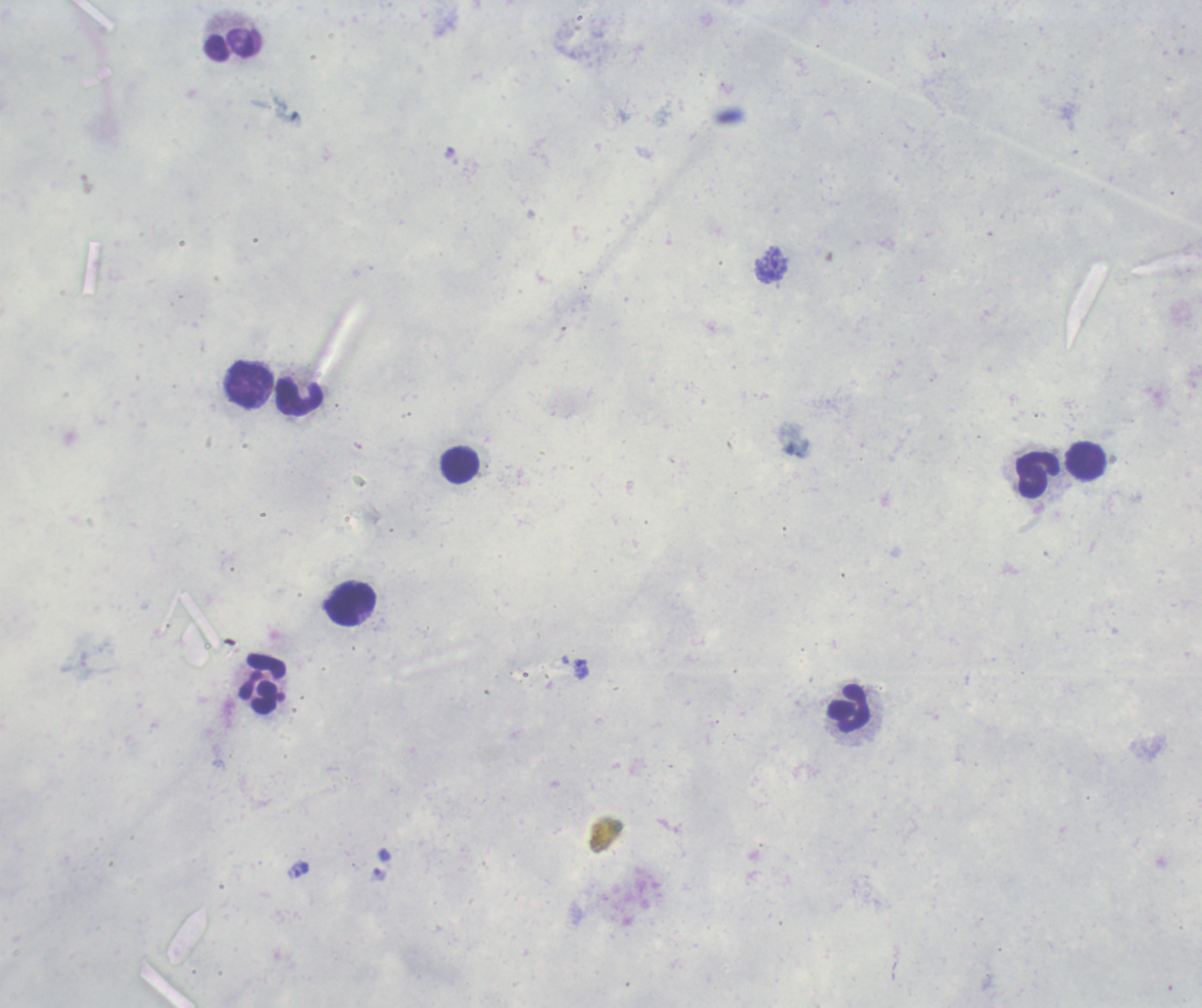

Approximate centers as {x, y} in pixels.
Summary:
  - Leukocyte locations: {233, 44}, {250, 385}, {300, 398}, {1086, 460}, {460, 465}, {1038, 474}, {351, 603}, {263, 683}, {849, 708}
  - Trophozoite locations: {771, 264}, {581, 668}, {298, 870}
  - Field of view: one from this slide
  - Context: previously used in a real diagnosis
  - Stain: Romanowsky
  - Preparation: thick smear of blood
  - Magnification: 100x
  - Result: Plasmodium parasites detected
  - Background quality: unsatisfactory
  - Image size: 1202×1008 pixels